Identify the parasite.
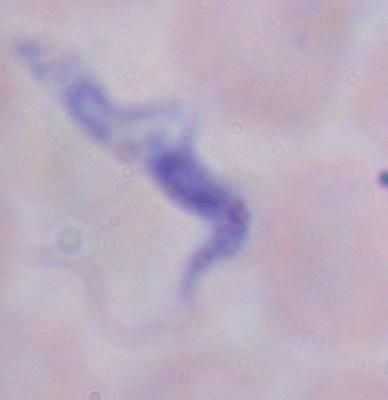
A trypanosome.

Captured at 1000x magnification. Micrograph.